Assess the morphology of the erythrocytes.
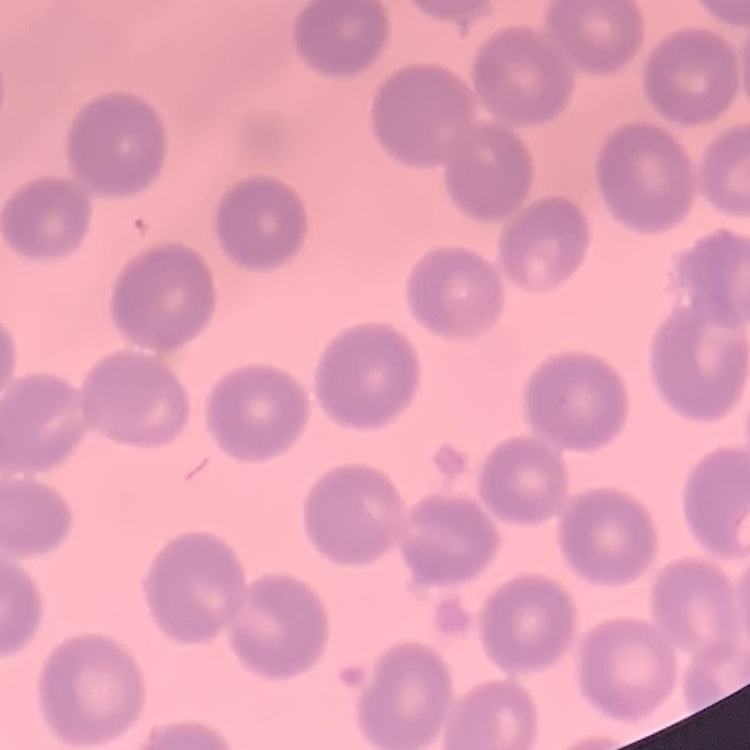

They show no rouleaux formation.

Summary:
  - Image type: one tile cut from a larger photomicrograph
  - Stain: Field's or Giemsa
  - Preparation: thin blood smear